Mark where platelets are.
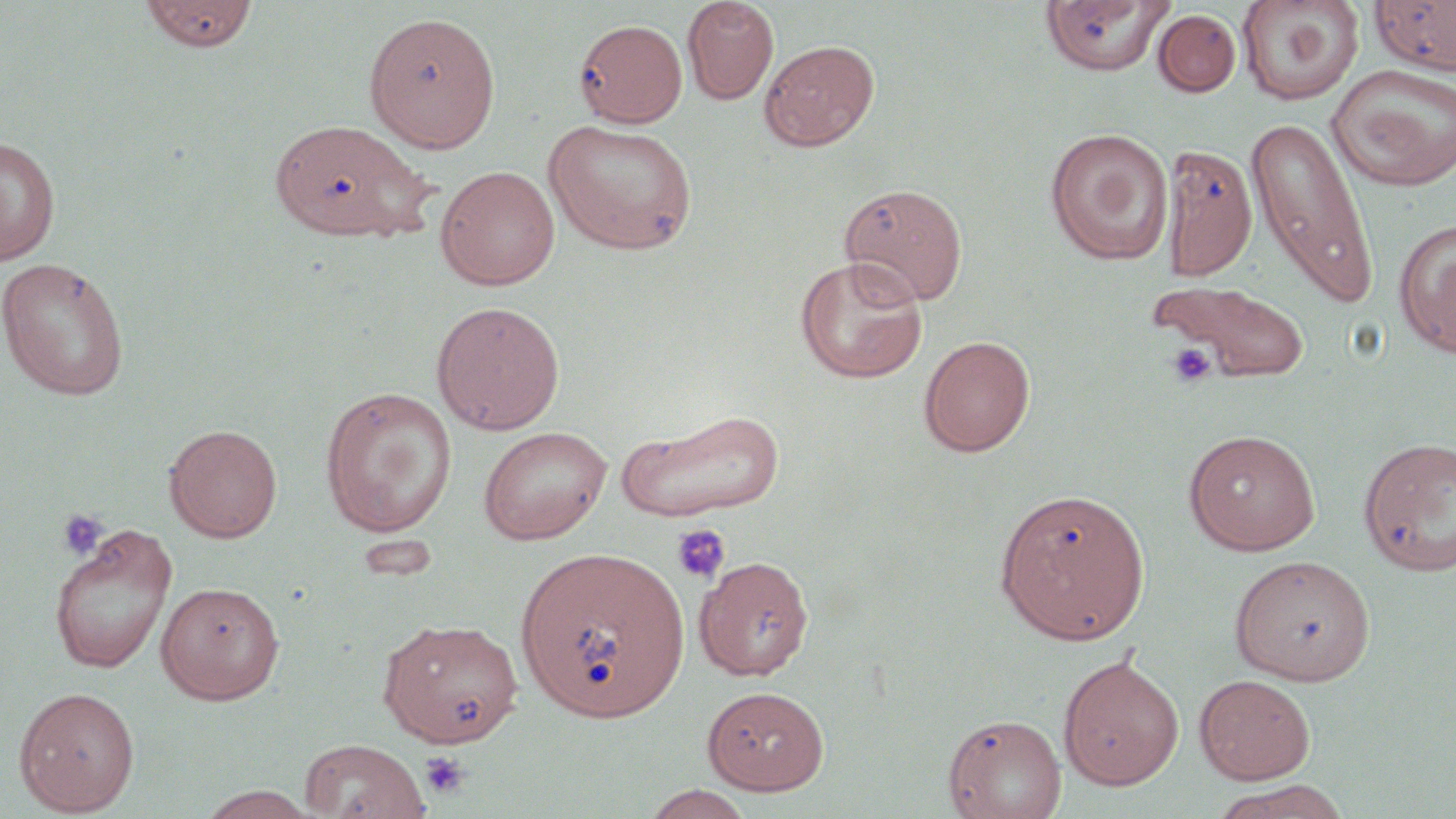
Approximate bounding boxes as named x1/y1/x2/y2 corners in pixels.
Platelets: (x1=1166, y1=343, x2=1216, y2=387), (x1=55, y1=509, x2=110, y2=560), (x1=671, y1=523, x2=731, y2=584), (x1=419, y1=750, x2=471, y2=800).

Summary:
  - Uninfected red blood cell locations: (x1=138, y1=0, x2=259, y2=53), (x1=681, y1=0, x2=779, y2=104), (x1=1237, y1=0, x2=1364, y2=106), (x1=1369, y1=0, x2=1456, y2=75), (x1=1039, y1=1, x2=1175, y2=76), (x1=1153, y1=9, x2=1241, y2=97), (x1=363, y1=11, x2=501, y2=153), (x1=573, y1=19, x2=688, y2=127), (x1=759, y1=39, x2=880, y2=151), (x1=1327, y1=64, x2=1456, y2=192), (x1=1245, y1=115, x2=1380, y2=310), (x1=268, y1=118, x2=434, y2=241), (x1=543, y1=119, x2=697, y2=255), (x1=1044, y1=127, x2=1174, y2=265), (x1=0, y1=135, x2=60, y2=266), (x1=1161, y1=144, x2=1258, y2=280), (x1=435, y1=165, x2=560, y2=291), (x1=838, y1=182, x2=968, y2=306), (x1=1394, y1=217, x2=1456, y2=358), (x1=794, y1=255, x2=929, y2=383), (x1=0, y1=257, x2=131, y2=401), (x1=1148, y1=278, x2=1314, y2=385), (x1=430, y1=300, x2=565, y2=435), (x1=918, y1=334, x2=1036, y2=457), (x1=319, y1=386, x2=457, y2=537), (x1=616, y1=407, x2=786, y2=523), (x1=164, y1=424, x2=283, y2=543), (x1=478, y1=426, x2=612, y2=544), (x1=1183, y1=429, x2=1320, y2=555), (x1=1357, y1=435, x2=1455, y2=576), (x1=993, y1=486, x2=1151, y2=645), (x1=48, y1=522, x2=178, y2=674), (x1=515, y1=545, x2=690, y2=723), (x1=694, y1=554, x2=815, y2=680), (x1=1229, y1=554, x2=1375, y2=686), (x1=154, y1=581, x2=284, y2=703), (x1=377, y1=618, x2=524, y2=748), (x1=1058, y1=654, x2=1184, y2=791), (x1=1194, y1=674, x2=1315, y2=785), (x1=702, y1=685, x2=829, y2=795), (x1=13, y1=686, x2=140, y2=815), (x1=942, y1=713, x2=1067, y2=819), (x1=298, y1=738, x2=430, y2=818), (x1=1211, y1=780, x2=1352, y2=819), (x1=641, y1=784, x2=756, y2=819), (x1=196, y1=785, x2=319, y2=819)
  - Slide-level diagnosis: no evidence of blood parasites
  - Modality: light microscopy
  - Magnification: 1000x
  - Stain: May-Grünwald-Giemsa
  - Preparation: thin blood smear
  - Image size: 1456×819 pixels
  - Field of view: single